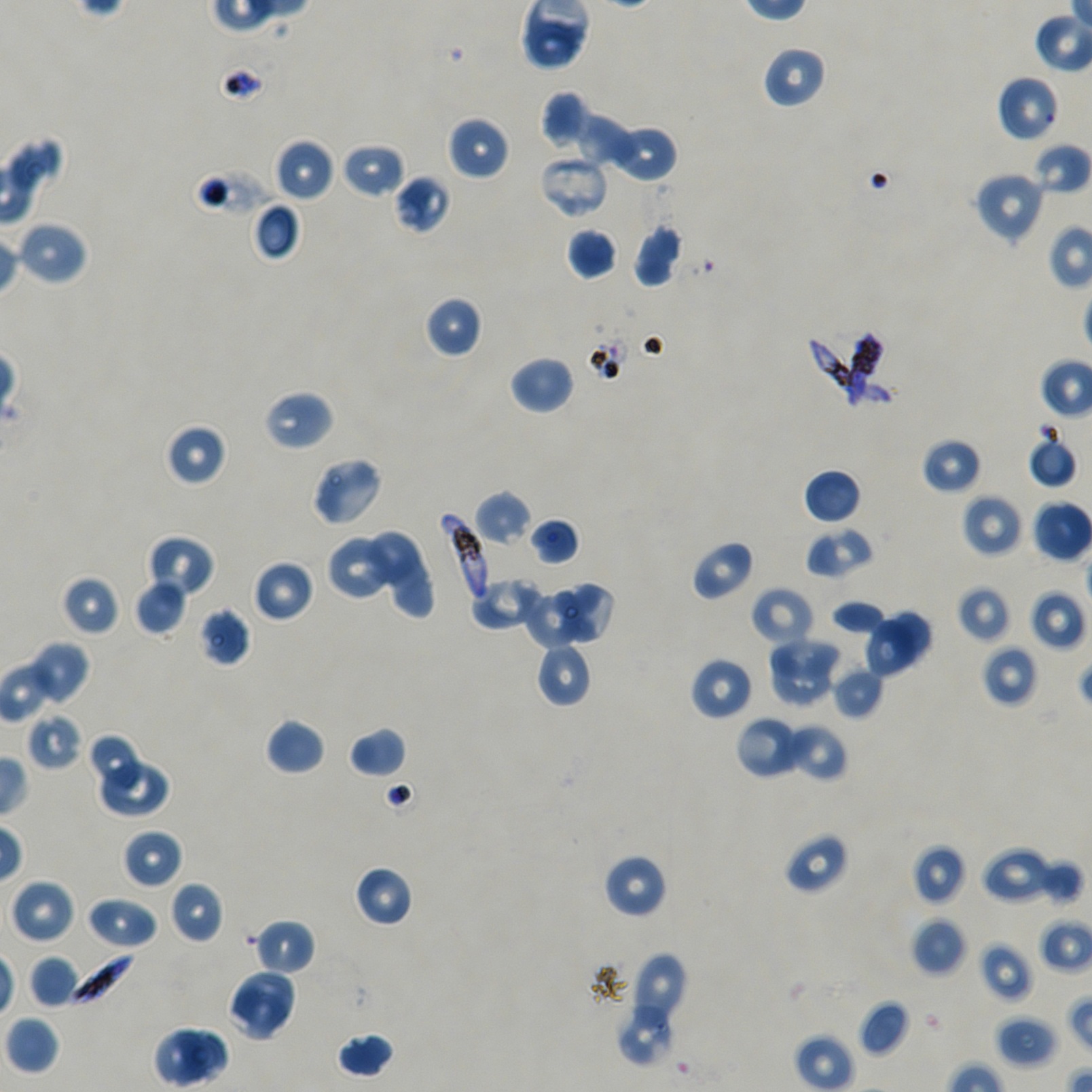

Approximate bounding boxes as (x1, y1, x2, y2) in pixels. Not every red blood cell is marked. Locations of uninfected red blood cells: (763, 45, 827, 109), (996, 75, 1060, 143), (539, 90, 590, 151), (573, 111, 637, 170), (447, 115, 509, 181), (606, 125, 678, 183), (273, 138, 335, 202), (1032, 141, 1091, 196), (341, 143, 405, 199), (972, 170, 1046, 244), (394, 174, 452, 236), (251, 202, 302, 263), (14, 220, 89, 286), (632, 223, 685, 288), (566, 227, 618, 280), (424, 295, 484, 358), (509, 355, 575, 415), (263, 390, 334, 452), (164, 422, 228, 487), (1027, 433, 1078, 489), (921, 437, 982, 495), (310, 457, 384, 527), (803, 468, 862, 525), (473, 490, 532, 547), (962, 493, 1025, 558), (1031, 498, 1092, 563), (528, 517, 581, 565), (805, 527, 874, 579), (365, 530, 421, 585), (147, 534, 215, 599), (327, 534, 398, 602), (690, 540, 754, 602), (388, 554, 437, 620), (252, 559, 314, 623), (60, 574, 120, 638), (469, 577, 543, 632), (134, 579, 187, 636), (553, 582, 616, 645), (956, 585, 1011, 644), (750, 586, 815, 647), (1028, 588, 1087, 651), (523, 589, 583, 649), (830, 599, 888, 636), (884, 606, 934, 663), (198, 608, 251, 668), (861, 617, 920, 678), (765, 636, 843, 684), (26, 640, 91, 706), (534, 642, 592, 708), (982, 644, 1039, 707), (689, 656, 753, 721), (769, 657, 839, 708), (831, 665, 885, 719), (26, 712, 84, 771), (735, 716, 805, 780), (264, 717, 326, 776), (784, 723, 849, 783), (348, 726, 406, 778), (87, 733, 147, 795), (96, 758, 170, 818), (122, 828, 183, 889), (784, 832, 850, 895), (911, 844, 966, 906), (981, 846, 1055, 905), (602, 853, 668, 919), (1034, 857, 1085, 907), (354, 864, 414, 927), (10, 879, 75, 945), (168, 880, 224, 945), (86, 896, 158, 949), (911, 917, 967, 977), (253, 918, 316, 977), (979, 941, 1033, 1002), (621, 951, 687, 1044), (28, 955, 81, 1008), (231, 968, 297, 1026), (224, 986, 287, 1041), (858, 998, 911, 1057), (614, 1004, 675, 1069), (3, 1015, 61, 1076), (996, 1015, 1057, 1068), (153, 1025, 230, 1087), (335, 1032, 396, 1078). Locations of red blood cells of indeterminate infection status: (538, 155, 610, 219), (192, 168, 271, 219), (847, 331, 883, 413). Locations of infected red blood cells: (805, 335, 898, 410), (440, 513, 490, 606), (60, 948, 136, 1008). Single field of view. 100x oil-immersion objective, numerical aperture 1.45. Giemsa stain. Thin blood smear. Plasmodium falciparum strain NF54 in static in-vitro culture. Image is 1092×1092 pixels. Donor blood group A+/O+.